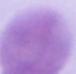
Summary:
  - Magnification: 1000x
  - Identification: erythrocyte
  - Modality: photomicrograph